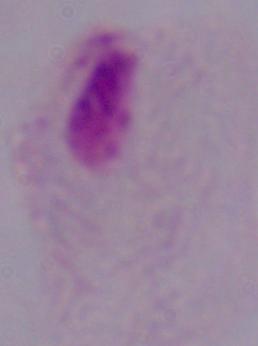

Summary:
  - Magnification: 1000x
  - Identification: trichomonad
  - Modality: photomicrograph